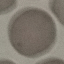 Malaria status: uninfected. Photographed with a smartphone camera at the microscope eyepiece. Automatically extracted cell patch, resized to 64 × 64 pixels. Thin blood film. Giemsa stain.